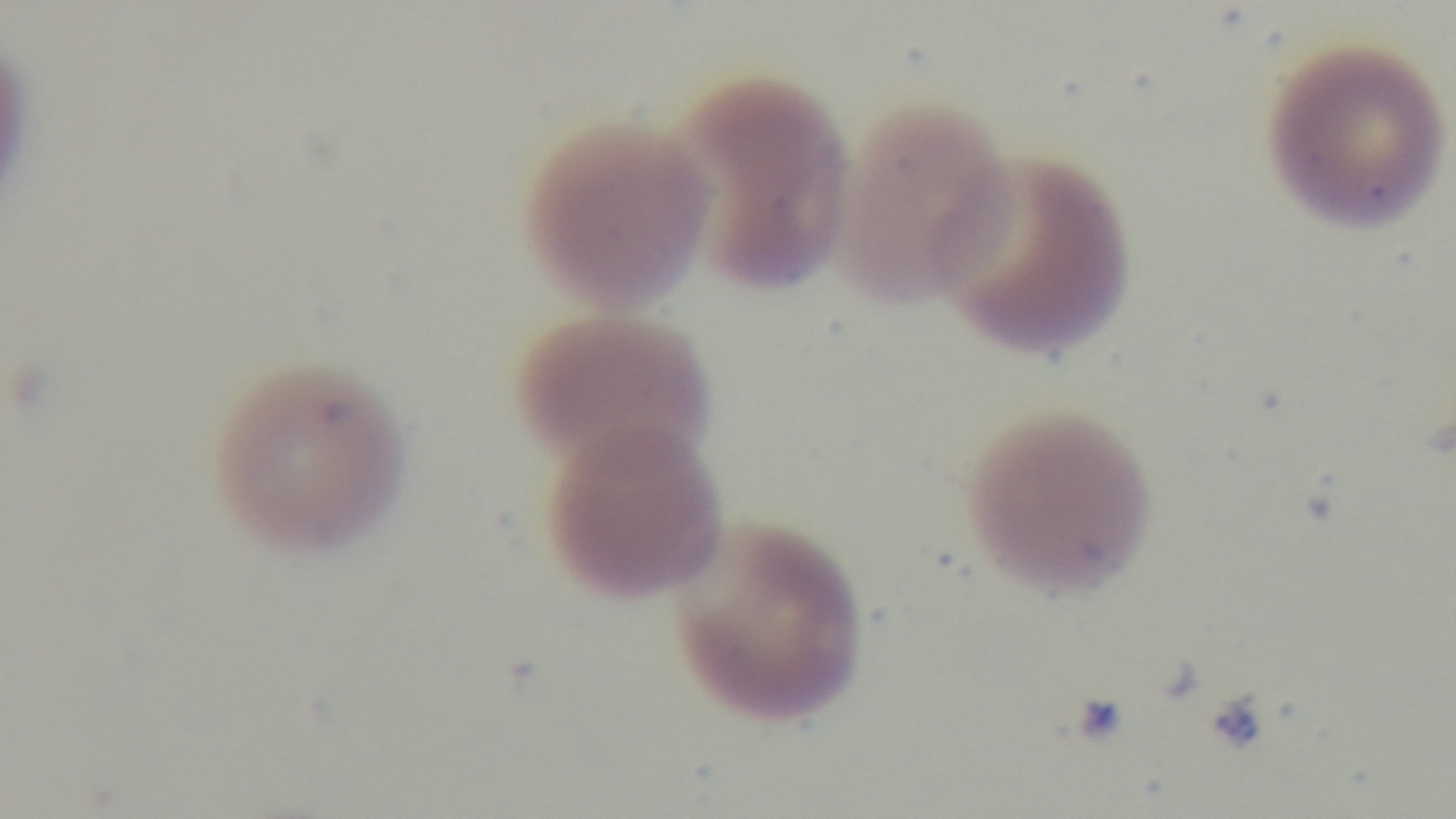

Summary:
  - Stain: Giemsa
  - Preparation: thin blood film
  - Objective: 100x oil immersion
  - Field of view: one from the slide
  - Capture: mounted 4K digital camera
  - Malaria status: positive
  - Modality: light microscopy